Comment on the morphology of the red blood cells.
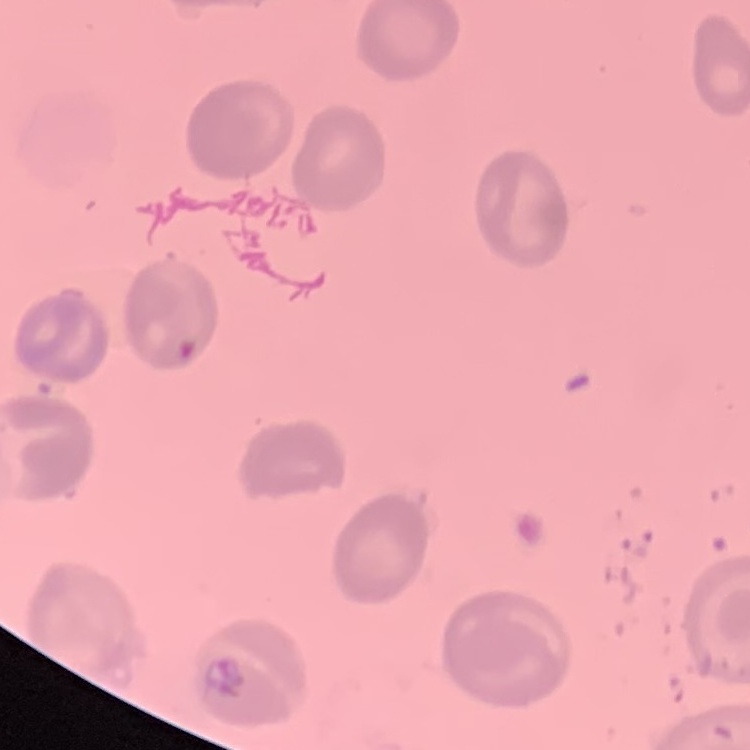

No rouleaux formation.

Summary:
  - Preparation: thin blood film
  - Image type: square crop of a larger photomicrograph
  - Stain: Field's or Giemsa